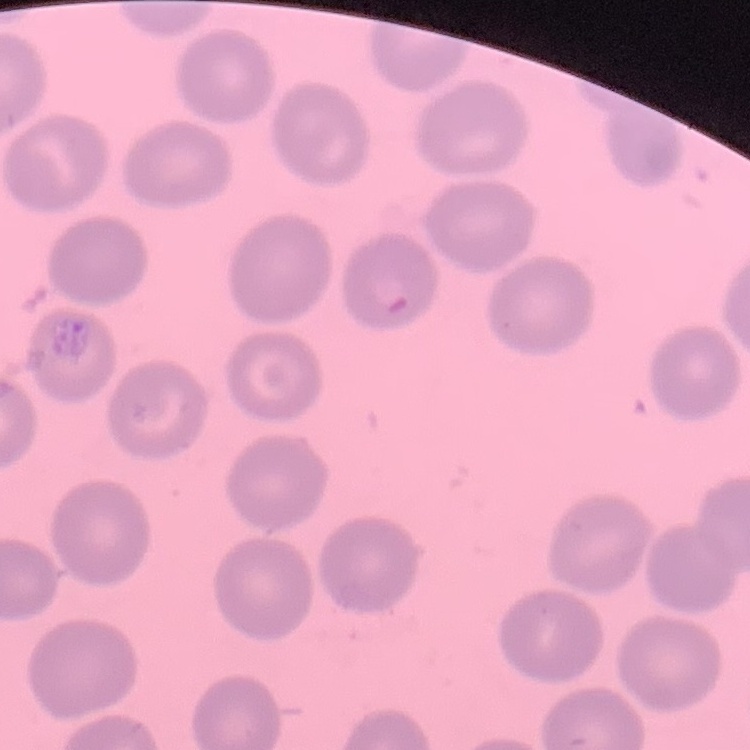

red_blood_cell_morphology: no rouleaux formation
image_type: square crop of a larger photomicrograph
stain: Field's or Giemsa
preparation: thin blood smear